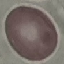
Result: no malaria parasites seen. Photographed with a smartphone camera at the microscope eyepiece. Automatically extracted cell patch, resized to 64 × 64 pixels. Giemsa-stained preparation. Thin blood film.